Comment on the morphology of the red blood cells.
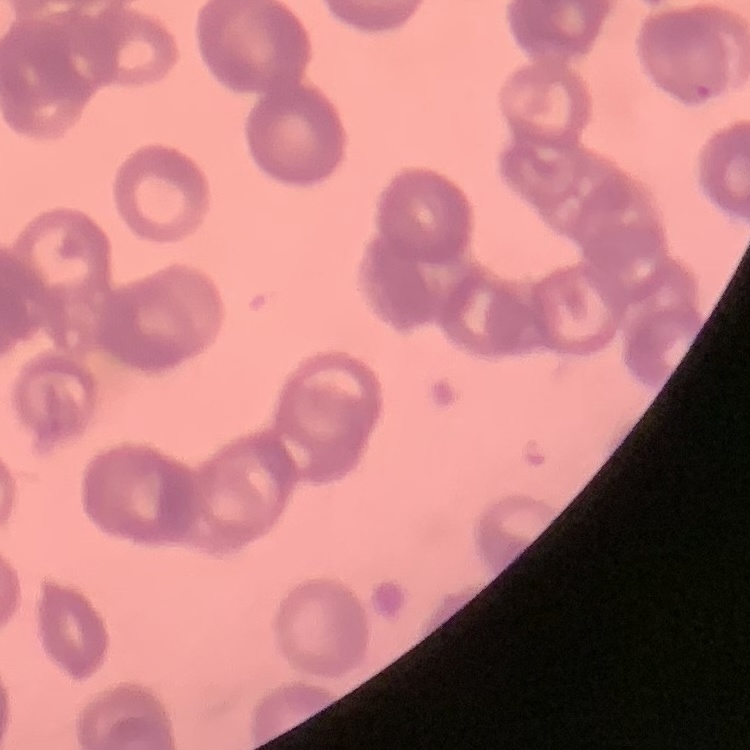

They show rouleaux formation.

stain: Field's or Giemsa
preparation: thin blood smear
image_type: square crop of a larger photomicrograph